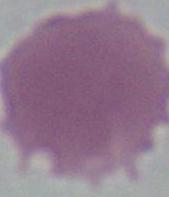
Summary:
  - Identification: red blood cell
  - Modality: photomicrograph
  - Magnification: 1000x